Identify the blood parasite species.
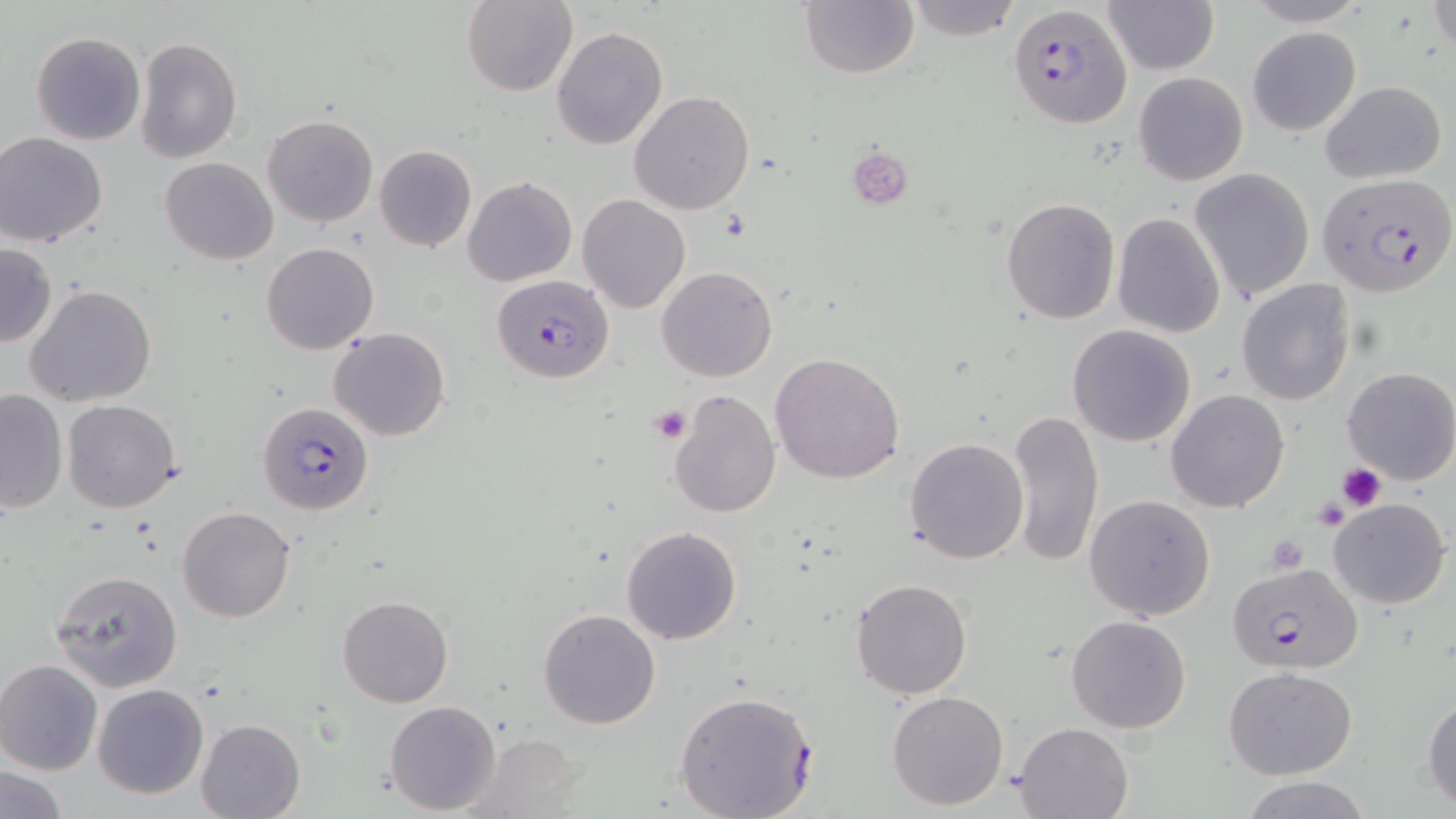
Plasmodium falciparum.

Summary:
  - Coordinate format: approximate bounding boxes as named x1/y1/x2/y2 corners in pixels
  - Platelet locations: (x1=846, y1=147, x2=912, y2=209), (x1=649, y1=404, x2=691, y2=444), (x1=1336, y1=463, x2=1386, y2=511), (x1=1312, y1=497, x2=1351, y2=532), (x1=1265, y1=535, x2=1309, y2=572)
  - Plasmodium falciparum-infected red blood cell locations: (x1=1006, y1=4, x2=1132, y2=129), (x1=1318, y1=172, x2=1456, y2=298), (x1=493, y1=274, x2=611, y2=385), (x1=257, y1=401, x2=373, y2=514), (x1=1228, y1=561, x2=1363, y2=673), (x1=673, y1=690, x2=818, y2=817)
  - Uninfected red blood cell locations: (x1=900, y1=0, x2=1027, y2=41), (x1=1244, y1=0, x2=1372, y2=27), (x1=461, y1=1, x2=579, y2=97), (x1=801, y1=1, x2=918, y2=79), (x1=1101, y1=1, x2=1220, y2=77), (x1=1428, y1=1, x2=1455, y2=57), (x1=551, y1=26, x2=668, y2=149), (x1=1247, y1=27, x2=1361, y2=134), (x1=31, y1=31, x2=146, y2=146), (x1=135, y1=36, x2=242, y2=165), (x1=1132, y1=72, x2=1248, y2=186), (x1=1319, y1=79, x2=1448, y2=183), (x1=627, y1=90, x2=756, y2=214), (x1=262, y1=114, x2=378, y2=227), (x1=0, y1=133, x2=106, y2=246), (x1=373, y1=145, x2=476, y2=252), (x1=160, y1=157, x2=278, y2=266), (x1=1190, y1=167, x2=1314, y2=303), (x1=463, y1=177, x2=577, y2=287), (x1=577, y1=195, x2=689, y2=314), (x1=1001, y1=198, x2=1121, y2=323), (x1=1111, y1=214, x2=1226, y2=338), (x1=261, y1=241, x2=379, y2=355), (x1=0, y1=242, x2=57, y2=346), (x1=658, y1=265, x2=779, y2=382), (x1=1236, y1=279, x2=1355, y2=407), (x1=26, y1=284, x2=157, y2=408), (x1=1067, y1=325, x2=1197, y2=448), (x1=329, y1=328, x2=451, y2=442), (x1=770, y1=351, x2=905, y2=483), (x1=1341, y1=366, x2=1456, y2=485), (x1=667, y1=388, x2=780, y2=518), (x1=0, y1=389, x2=68, y2=513), (x1=1166, y1=389, x2=1291, y2=513), (x1=63, y1=399, x2=181, y2=513), (x1=1007, y1=408, x2=1103, y2=570), (x1=903, y1=437, x2=1030, y2=565), (x1=1084, y1=493, x2=1217, y2=620), (x1=1329, y1=497, x2=1452, y2=608), (x1=177, y1=507, x2=297, y2=623), (x1=621, y1=525, x2=743, y2=645), (x1=51, y1=570, x2=182, y2=691), (x1=850, y1=577, x2=972, y2=700), (x1=337, y1=595, x2=453, y2=707), (x1=537, y1=607, x2=662, y2=730), (x1=1065, y1=614, x2=1192, y2=734), (x1=0, y1=659, x2=103, y2=775), (x1=1224, y1=666, x2=1357, y2=780), (x1=94, y1=684, x2=208, y2=799), (x1=886, y1=690, x2=1009, y2=811), (x1=1421, y1=691, x2=1456, y2=810), (x1=384, y1=700, x2=501, y2=815), (x1=196, y1=718, x2=305, y2=819), (x1=1014, y1=722, x2=1132, y2=818), (x1=474, y1=732, x2=585, y2=817), (x1=1, y1=766, x2=69, y2=818), (x1=1239, y1=774, x2=1372, y2=819)
  - Field of view: one of a larger specimen
  - Modality: light microscopy
  - Magnification: 1000x
  - Preparation: thin blood film
  - Image size: 1456×819 pixels
  - Stain: May-Grünwald-Giemsa